Report the malaria status of this cell.
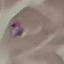
Parasitized.

{
  "stain": "Giemsa",
  "capture": "smartphone camera at the microscope eyepiece",
  "image_type": "cell patch, automatically extracted from a larger field of view and resized to 64 × 64 pixels",
  "preparation": "thin blood smear"
}